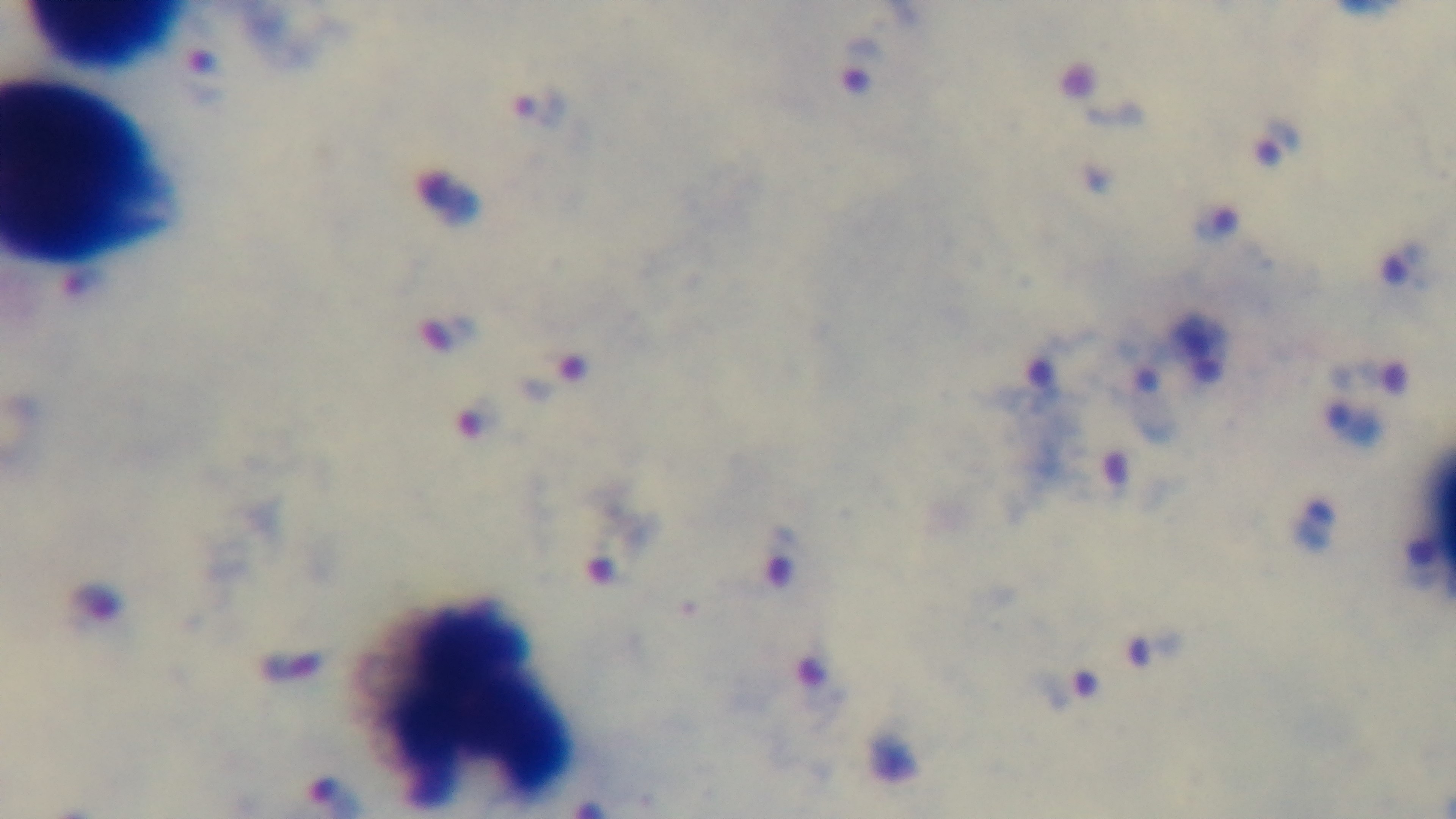

field_of_view: one from the slide
malaria_status: positive
objective: 100x oil immersion
capture: mounted 4K digital camera
preparation: thick blood film
stain: Giemsa
modality: light microscopy